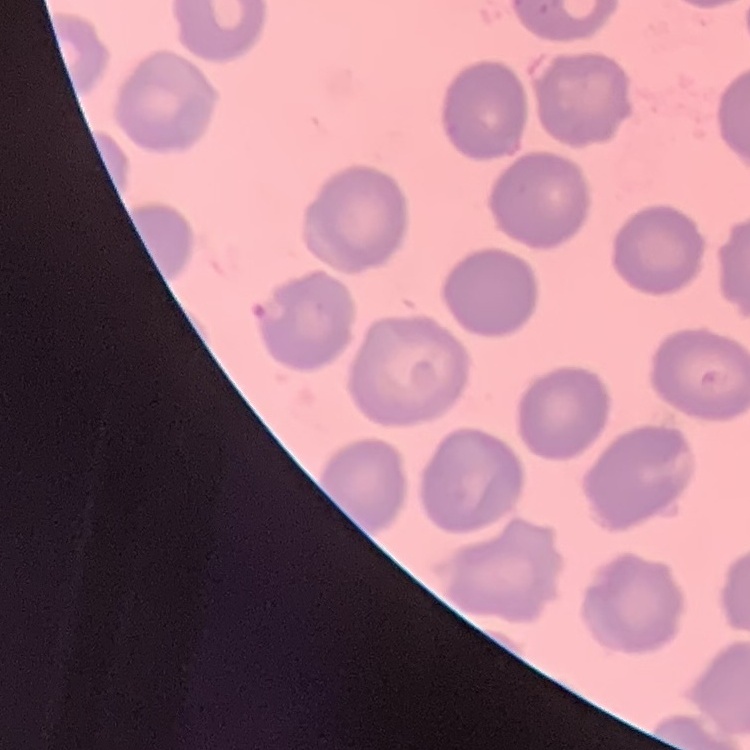
The red blood cells exhibit no rouleaux formation. One tile cut from a larger photomicrograph. Stained with either Field's or Giemsa. Thin peripheral smear.